Point out every malaria parasite and every leukocyte.
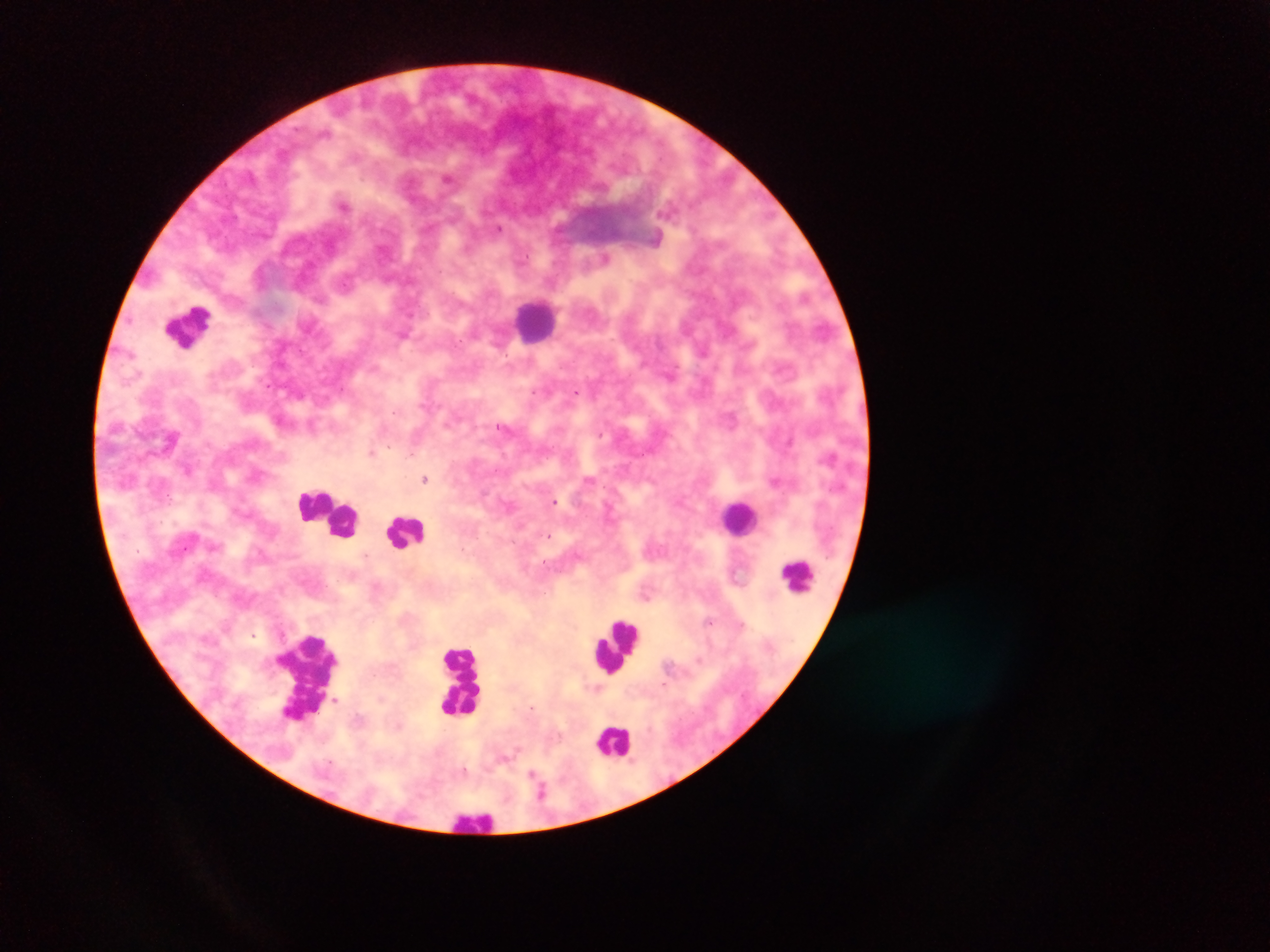
Approximate centers as x y in pixels.
Malaria parasites: 448 179; 344 205; 499 228; 605 258; 703 350; 670 375; 576 392; 394 413; 601 435; 371 452; 425 479; 775 481; 554 502; 549 536; 366 555; 710 622; 741 624; 254 635; 464 770; 536 780.
Leukocytes: 536 319; 188 324; 315 504; 332 515; 739 517; 407 530; 797 575; 617 642; 309 676; 462 677; 614 741; 474 819.

Mobile-phone photograph taken through the microscope. Image is 1270×952 pixels. Sample from Ghana. Thick blood film. One field of view.